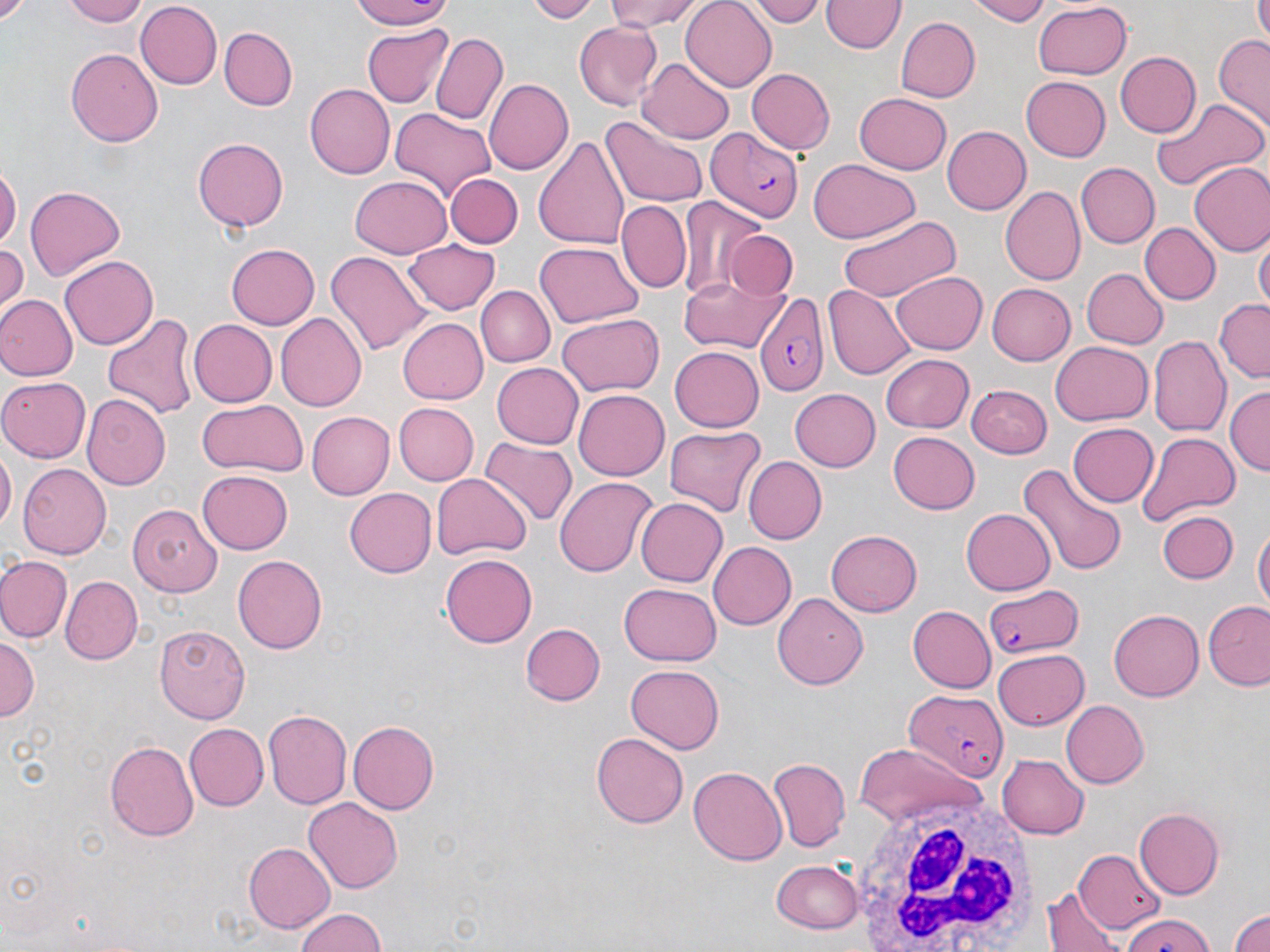
slide-level diagnosis = Plasmodium falciparum
image size = 1270×952 pixels
field of view = one of a larger specimen
white blood cell locations = approximate bounding boxes as [x1, y1, x2, y2] in pixels: [845, 787, 1040, 952]
uninfected red blood cell locations = approximate bounding boxes as [x1, y1, x2, y2] in pixels: [60, 0, 150, 26], [348, 0, 460, 27], [525, 0, 604, 22], [604, 0, 709, 28], [745, 0, 828, 25], [963, 0, 1055, 24], [1255, 0, 1270, 40], [680, 1, 777, 90], [821, 1, 904, 55], [136, 2, 222, 90], [1031, 2, 1132, 81], [896, 17, 980, 102], [573, 20, 663, 110], [361, 24, 451, 106], [221, 28, 297, 110], [429, 30, 508, 124], [1213, 34, 1270, 131], [66, 49, 164, 146], [1115, 52, 1201, 138], [641, 57, 735, 142], [746, 68, 835, 155], [1022, 75, 1111, 162], [483, 77, 574, 174], [305, 83, 396, 178], [854, 91, 953, 173], [1151, 97, 1267, 191], [391, 108, 497, 201], [603, 117, 708, 210], [941, 125, 1031, 215], [192, 136, 290, 232], [534, 136, 630, 252], [806, 159, 919, 244], [0, 161, 19, 249], [1076, 162, 1159, 247], [1188, 163, 1270, 256], [446, 173, 522, 248], [350, 174, 451, 258], [25, 186, 126, 281], [999, 186, 1085, 286], [678, 197, 770, 299], [619, 200, 691, 293], [836, 214, 962, 302], [1140, 223, 1220, 304], [725, 230, 799, 298], [404, 236, 501, 312], [1254, 236, 1269, 311], [536, 241, 644, 328], [0, 242, 25, 312], [226, 243, 320, 329], [325, 251, 430, 355], [60, 255, 158, 350], [1082, 267, 1167, 347], [681, 270, 786, 353], [890, 270, 988, 355], [983, 282, 1075, 367], [824, 284, 912, 380], [475, 285, 555, 367], [0, 296, 76, 382], [1213, 300, 1269, 382], [101, 311, 198, 421], [276, 312, 368, 412], [556, 313, 662, 397], [187, 319, 276, 408], [397, 319, 489, 405], [1149, 337, 1230, 436], [1050, 342, 1153, 426], [668, 345, 763, 433], [880, 353, 974, 433], [490, 362, 585, 448], [0, 377, 91, 460], [967, 383, 1050, 458], [1225, 386, 1269, 473], [788, 388, 880, 472], [574, 389, 668, 482], [82, 393, 171, 489], [195, 400, 309, 478], [393, 402, 478, 486], [309, 412, 396, 499], [1069, 422, 1159, 508], [665, 427, 766, 516], [1136, 431, 1240, 524], [888, 432, 980, 515], [479, 439, 574, 529], [0, 448, 15, 534], [743, 456, 827, 546], [1018, 462, 1126, 578], [16, 463, 110, 559], [199, 471, 292, 554], [432, 473, 530, 562], [554, 477, 657, 580], [343, 487, 435, 577], [636, 499, 727, 587], [128, 503, 221, 596], [960, 507, 1055, 596], [1157, 511, 1239, 583], [1253, 524, 1269, 618], [826, 530, 923, 616], [709, 541, 796, 628], [232, 553, 326, 652], [440, 554, 537, 648], [0, 556, 71, 642], [61, 574, 142, 663], [620, 581, 722, 665], [772, 593, 868, 690], [1205, 601, 1270, 690], [907, 605, 995, 692], [1109, 607, 1204, 701], [519, 621, 605, 705], [155, 625, 248, 722], [0, 636, 38, 725], [992, 649, 1088, 728], [624, 664, 724, 755], [1059, 700, 1149, 789], [264, 710, 351, 810], [348, 721, 439, 814], [185, 724, 268, 810], [590, 732, 689, 828], [105, 741, 197, 842], [853, 742, 978, 829], [996, 753, 1088, 838], [768, 758, 851, 851], [688, 765, 787, 865], [302, 798, 404, 894], [1135, 808, 1224, 899], [245, 843, 335, 933], [1075, 849, 1165, 934], [772, 858, 861, 935], [1046, 887, 1122, 952], [1225, 904, 1270, 952], [292, 908, 390, 952], [1116, 916, 1218, 952]
stain = May-Grünwald-Giemsa
modality = light microscopy
magnification = 1000x
preparation = thin blood smear
Plasmodium falciparum-infected red blood cell locations = approximate bounding boxes as [x1, y1, x2, y2] in pixels: [707, 128, 806, 224], [752, 293, 830, 397], [981, 582, 1087, 659], [900, 684, 1009, 781]